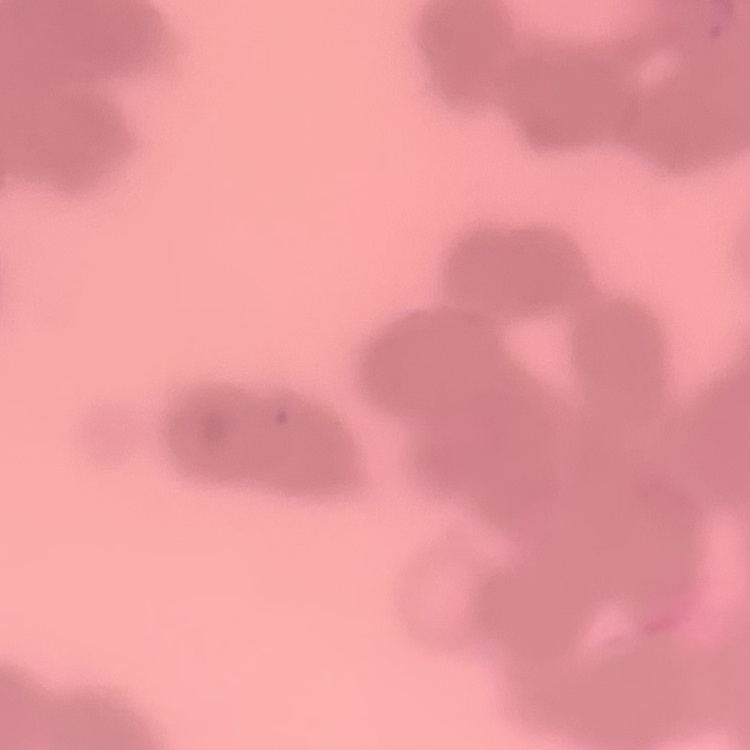
erythrocyte morphology = rouleaux formation
stain = Field's or Giemsa
preparation = thin peripheral smear
image type = one tile cut from a larger photomicrograph